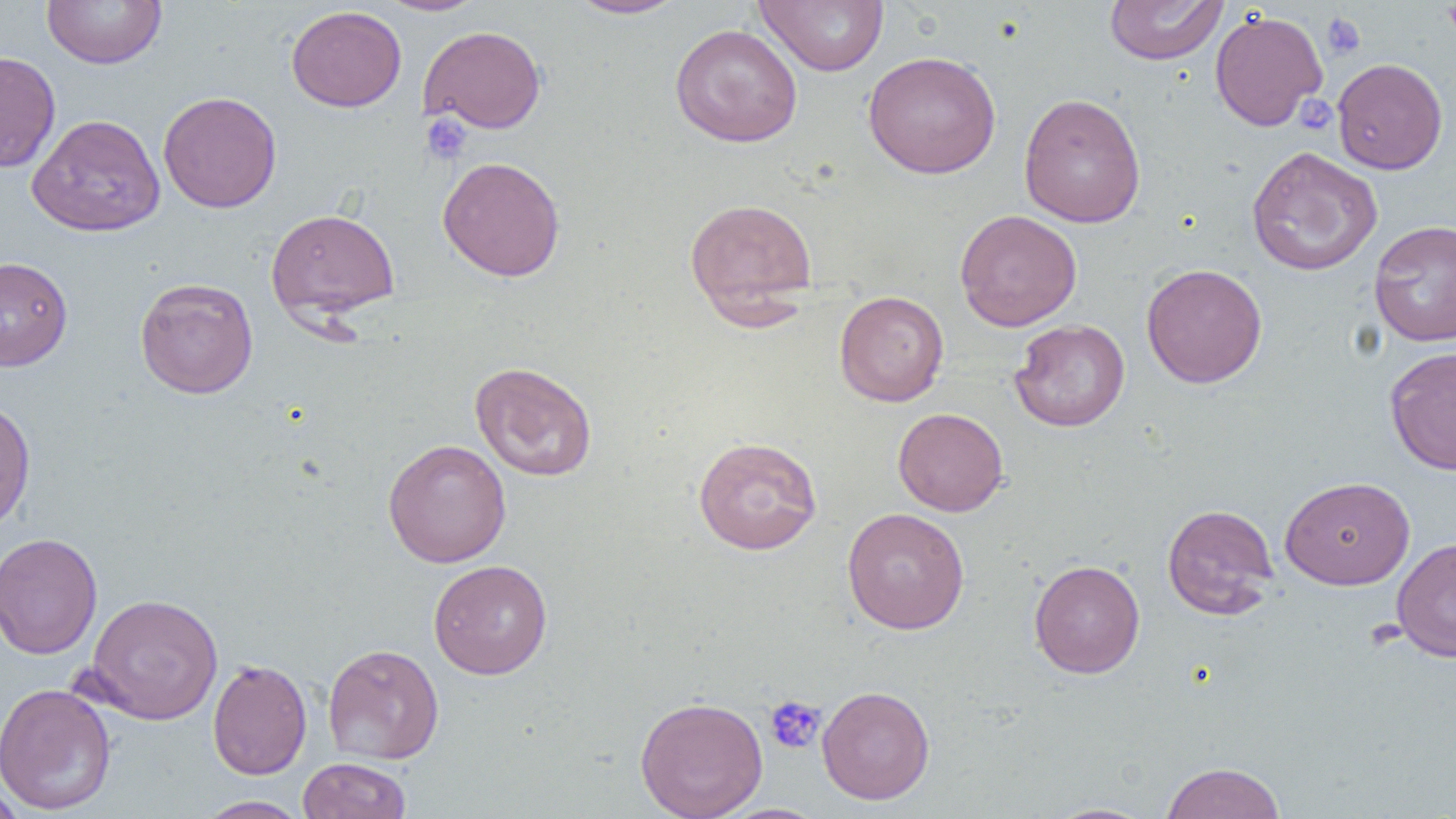
slide_level_diagnosis: no evidence of blood parasites
image_size: 1456×819 pixels
platelet_locations: 'approximate bounding boxes as [x1, y1, x2, y2] in pixels: [1322, 12, 1366, 59], [1296, 93, 1336, 136], [421, 114, 472, 164], [764, 695, 826, 754]'
preparation: thin blood smear
modality: optical microscopy
field_of_view: one of a larger specimen
uninfected_red_blood_cell_locations: 'approximate bounding boxes as [x1, y1, x2, y2] in pixels: [42, 0, 167, 69], [379, 0, 488, 16], [564, 0, 689, 19], [1104, 0, 1228, 65], [754, 1, 889, 75], [286, 5, 406, 112], [1209, 9, 1328, 131], [670, 23, 803, 147], [419, 25, 546, 133], [863, 50, 1001, 179], [0, 51, 61, 172], [1332, 58, 1447, 175], [158, 91, 282, 213], [1018, 92, 1146, 227], [27, 113, 166, 237], [1246, 145, 1383, 276], [437, 156, 566, 282], [684, 197, 818, 320], [266, 207, 400, 322], [955, 209, 1082, 332], [1368, 219, 1456, 347], [0, 256, 73, 371], [1141, 263, 1268, 388], [134, 277, 259, 399], [834, 290, 948, 406], [1009, 319, 1130, 432], [1385, 346, 1456, 475], [469, 361, 598, 481], [0, 397, 36, 533], [893, 407, 1008, 516], [693, 436, 822, 555], [382, 439, 511, 567], [1279, 475, 1415, 590], [1161, 503, 1279, 619], [842, 508, 970, 634], [0, 532, 103, 660], [1391, 536, 1456, 662], [428, 559, 553, 679], [1029, 559, 1145, 679], [85, 592, 223, 724], [322, 643, 444, 764], [208, 659, 312, 779], [0, 682, 116, 815], [817, 685, 935, 805], [635, 695, 768, 819], [297, 757, 411, 819], [1160, 761, 1287, 819], [0, 780, 27, 818], [195, 795, 312, 818], [1042, 802, 1159, 819]'
magnification: 1000x